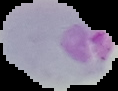

Summary:
  - Image size: 118×91 pixels
  - Result: Plasmodium parasites identified
  - Preparation: thin blood film
  - Image type: cell region segmented out of the field of view; surrounding area masked to black